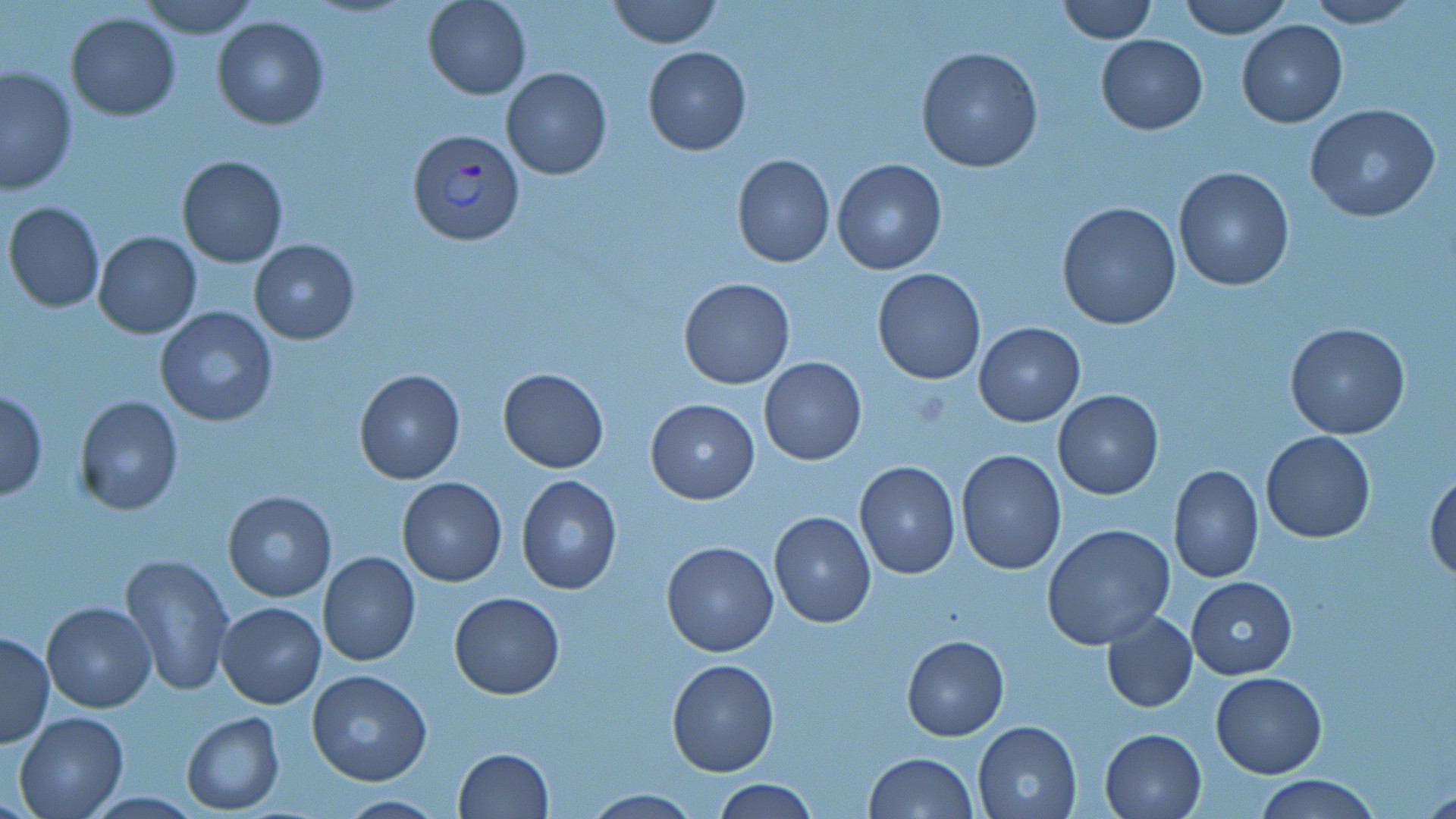

{
  "slide_level_diagnosis": "Plasmodium vivax",
  "magnification": "1000x",
  "field_of_view": "single",
  "stain": "May-Grünwald-Giemsa",
  "preparation": "thin blood film",
  "uninfected_red_blood_cell_locations": "approximate bounding boxes as [x1, y1, x2, y2] in pixels: [137, 0, 261, 39], [423, 0, 531, 99], [606, 0, 724, 49], [1056, 0, 1157, 43], [1178, 0, 1292, 38], [1301, 0, 1422, 27], [64, 12, 181, 120], [211, 17, 330, 129], [1236, 20, 1348, 128], [1095, 33, 1206, 133], [642, 46, 751, 156], [915, 46, 1043, 174], [1, 65, 76, 195], [501, 67, 612, 180], [1305, 102, 1440, 222], [731, 153, 835, 268], [176, 155, 288, 268], [832, 159, 947, 274], [1172, 167, 1295, 291], [4, 201, 105, 313], [1057, 202, 1182, 330], [92, 230, 201, 338], [249, 239, 359, 343], [872, 268, 987, 385], [678, 277, 795, 389], [154, 307, 277, 427], [1284, 321, 1412, 440], [974, 322, 1085, 426], [757, 357, 867, 466], [497, 367, 609, 474], [353, 369, 466, 484], [0, 389, 47, 501], [1052, 390, 1163, 499], [73, 396, 185, 516], [646, 398, 759, 504], [1261, 431, 1375, 543], [955, 448, 1066, 575], [854, 462, 961, 580], [1167, 464, 1263, 582], [1425, 466, 1456, 582], [516, 474, 621, 595], [396, 477, 507, 587], [222, 491, 337, 601], [769, 511, 876, 629], [1043, 523, 1176, 649], [661, 539, 780, 657], [318, 551, 421, 667], [120, 555, 234, 696], [1187, 576, 1297, 678], [448, 591, 564, 697], [42, 602, 156, 714], [216, 602, 326, 709], [1101, 610, 1198, 713], [1, 631, 54, 748], [902, 635, 1009, 739], [667, 657, 780, 776], [307, 670, 432, 786], [1211, 672, 1327, 777], [14, 712, 128, 819], [182, 712, 283, 813], [972, 719, 1084, 819], [1098, 727, 1206, 819], [453, 748, 554, 818], [864, 752, 979, 818], [1257, 774, 1378, 818], [712, 779, 820, 817], [580, 789, 701, 818], [333, 794, 453, 819]",
  "image_size": "1456×819 pixels",
  "plasmodium_vivax_infected_red_blood_cell_locations": "approximate bounding boxes as [x1, y1, x2, y2] in pixels: [406, 126, 523, 245]",
  "modality": "optical microscopy"
}